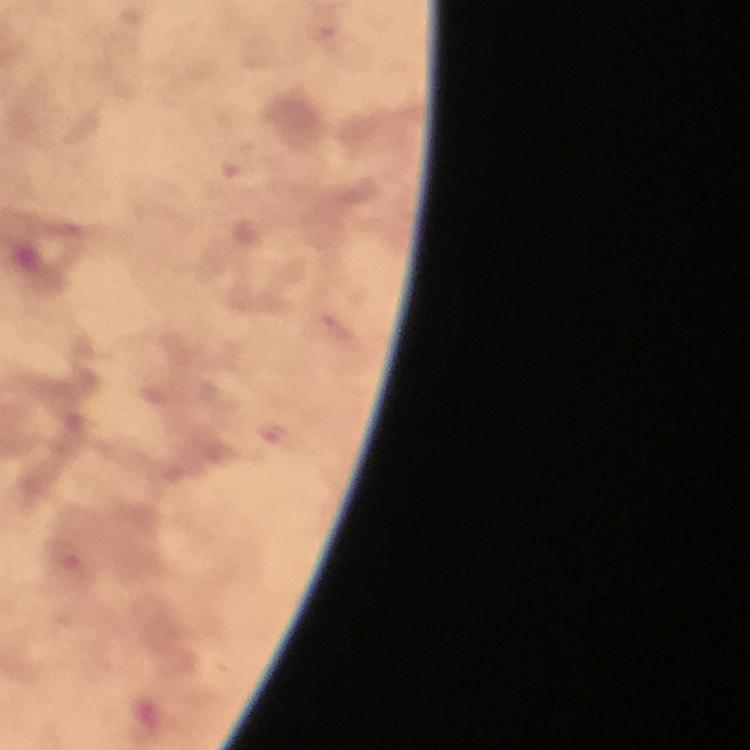

Approximate object centers, in pixels from the top-left corner.
Summary:
  - Malaria parasite locations: (x=328, y=37), (x=237, y=161)
  - Preparation: thick blood smear
  - Immersion oil: used
  - Capture: smartphone mounted on the microscope
  - Magnification: 100x
  - Stain: Giemsa
  - Cropped from: one field of view
  - Context: from a malaria diagnostic workup
  - Image size: 750×750 pixels